Comment on the morphology of the erythrocytes.
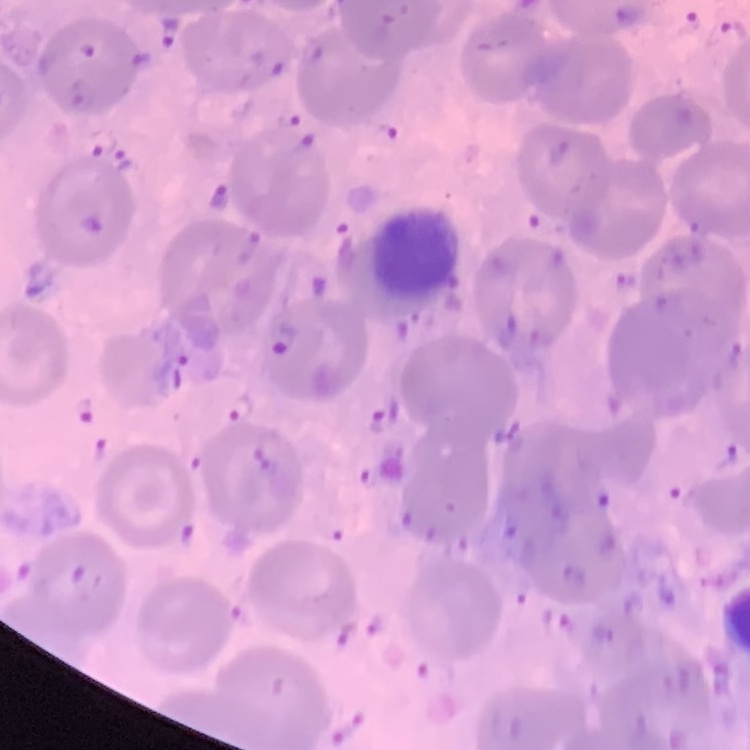

They show no rouleaux formation.

One tile cut from a larger photomicrograph. Stained with either Field's or Giemsa. Thin blood smear.